Assess this cell for malaria.
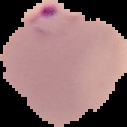
It is parasitized.

image type = segmented cell region with the area outside set to black
preparation = thin blood smear
image size = 127×127 pixels